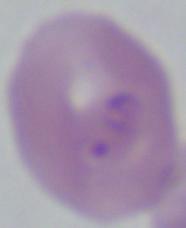
Captured at 1000x magnification. A Babesia parasite is shown. Micrograph.